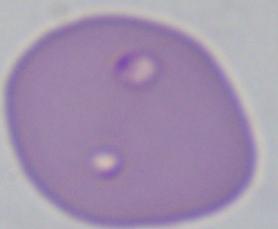
identification = Babesia
magnification = 1000x
modality = photomicrograph